Identify the parasite.
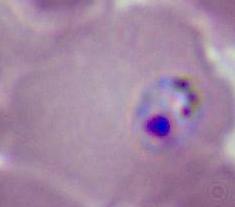

This is Plasmodium.

Captured at either 400x or 1000x magnification. Photomicrograph.